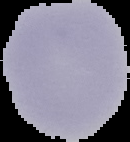

Segmented cell region on a black background. Image is 130×142 pixels. Malaria status: uninfected. From a thin blood smear.